Describe the morphology of the erythrocytes.
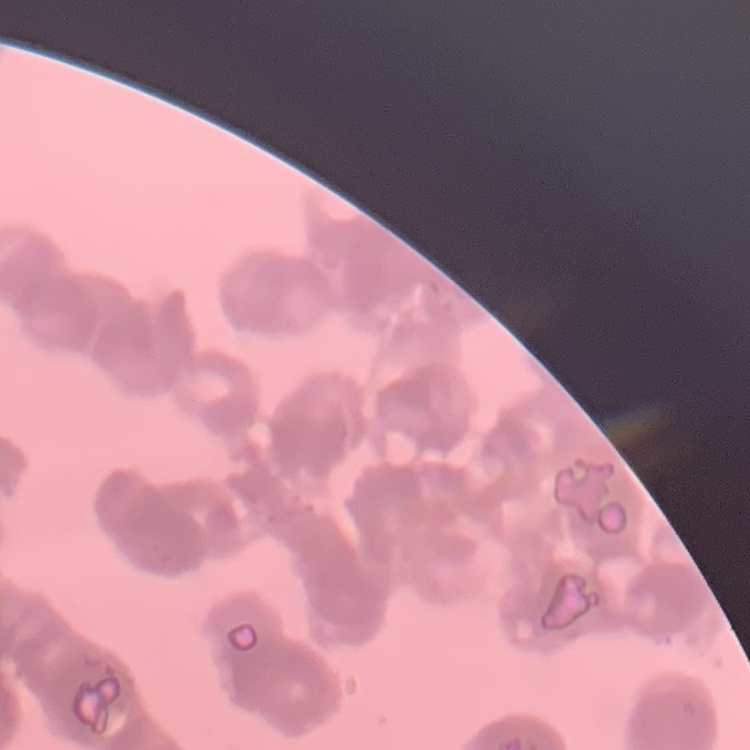
They show rouleaux formation.

Thin blood smear. One tile cut from a larger photomicrograph. Stained with either Field's or Giemsa.